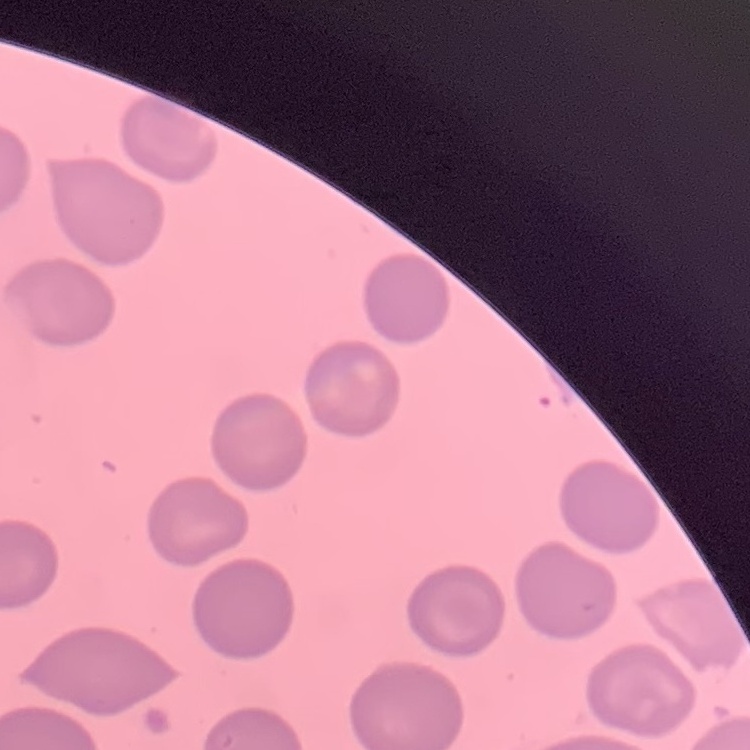
Summary:
  - Red blood cell morphology: no rouleaux formation
  - Image type: one tile cut from a larger photomicrograph
  - Preparation: thin peripheral smear
  - Stain: Field's or Giemsa